Describe the morphology of the erythrocytes.
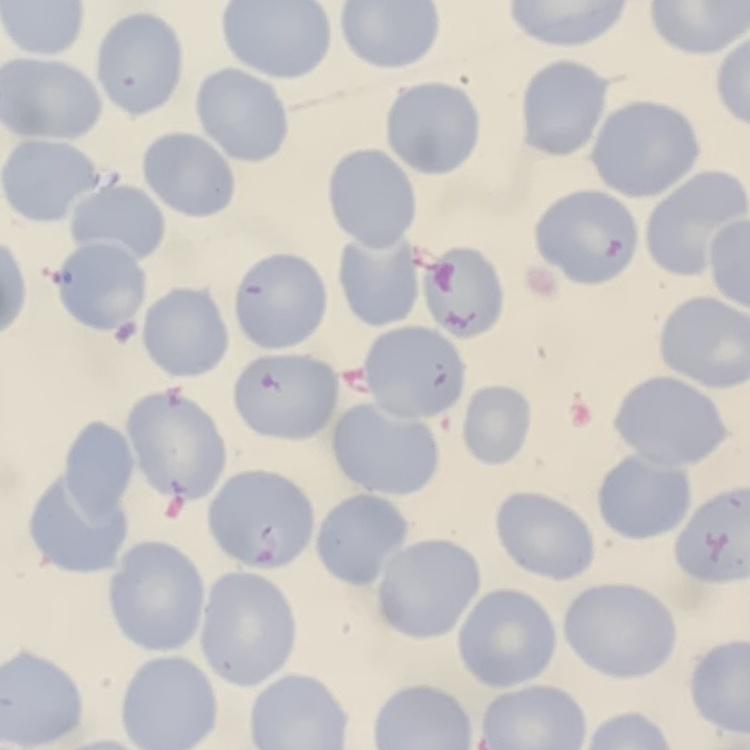

They show no rouleaux formation.

Thin blood film. Field's or Giemsa stain. One tile cut from a larger photomicrograph.